Name the parasite shown.
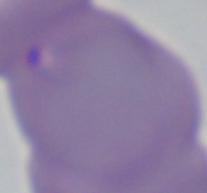
This is Babesia.

1000x magnification. Photomicrograph.